Assess this cell for malaria.
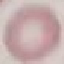
Uninfected.

{
  "image_type": "cell patch, automatically extracted from a larger field of view and resized to 64 × 64 pixels",
  "capture": "smartphone camera at the microscope eyepiece",
  "stain": "Giemsa",
  "preparation": "thin blood film"
}